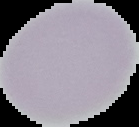
preparation = thin blood smear
malaria status = uninfected
image type = segmented cell region with the area outside set to black
image size = 139×127 pixels